Report the malaria status of this cell.
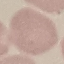

It is uninfected.

Summary:
  - Image type: automatically extracted cell patch, resized to 64 × 64 pixels
  - Stain: Giemsa
  - Capture: smartphone camera at the microscope eyepiece
  - Preparation: thin blood smear